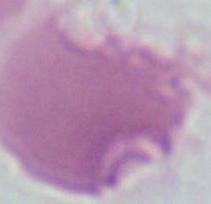

Micrograph. A red blood cell is shown. 1000x magnification.